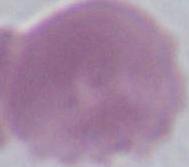

Summary:
  - Identification: red blood cell
  - Modality: micrograph
  - Magnification: 1000x